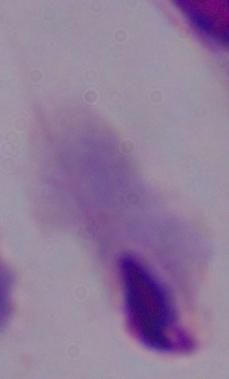

Summary:
  - Magnification: 1000x
  - Identification: trichomonad
  - Modality: photomicrograph